Classify this cell by malaria status.
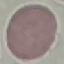

It is uninfected.

Summary:
  - Preparation: thin smear
  - Stain: Giemsa
  - Image type: cell patch, automatically extracted from a larger field of view and resized to 64 × 64 pixels
  - Capture: smartphone through the microscope eyepiece